Comment on the morphology of the erythrocytes.
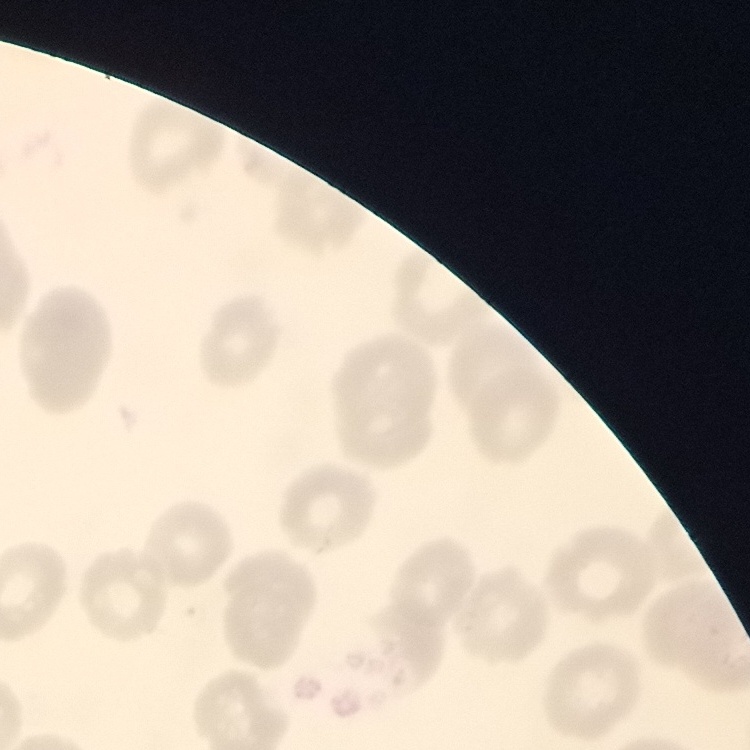
They show no rouleaux formation.

image type = one tile cut from a larger photomicrograph
stain = Field's or Giemsa
preparation = thin peripheral smear